Give the position of every malaria parasite.
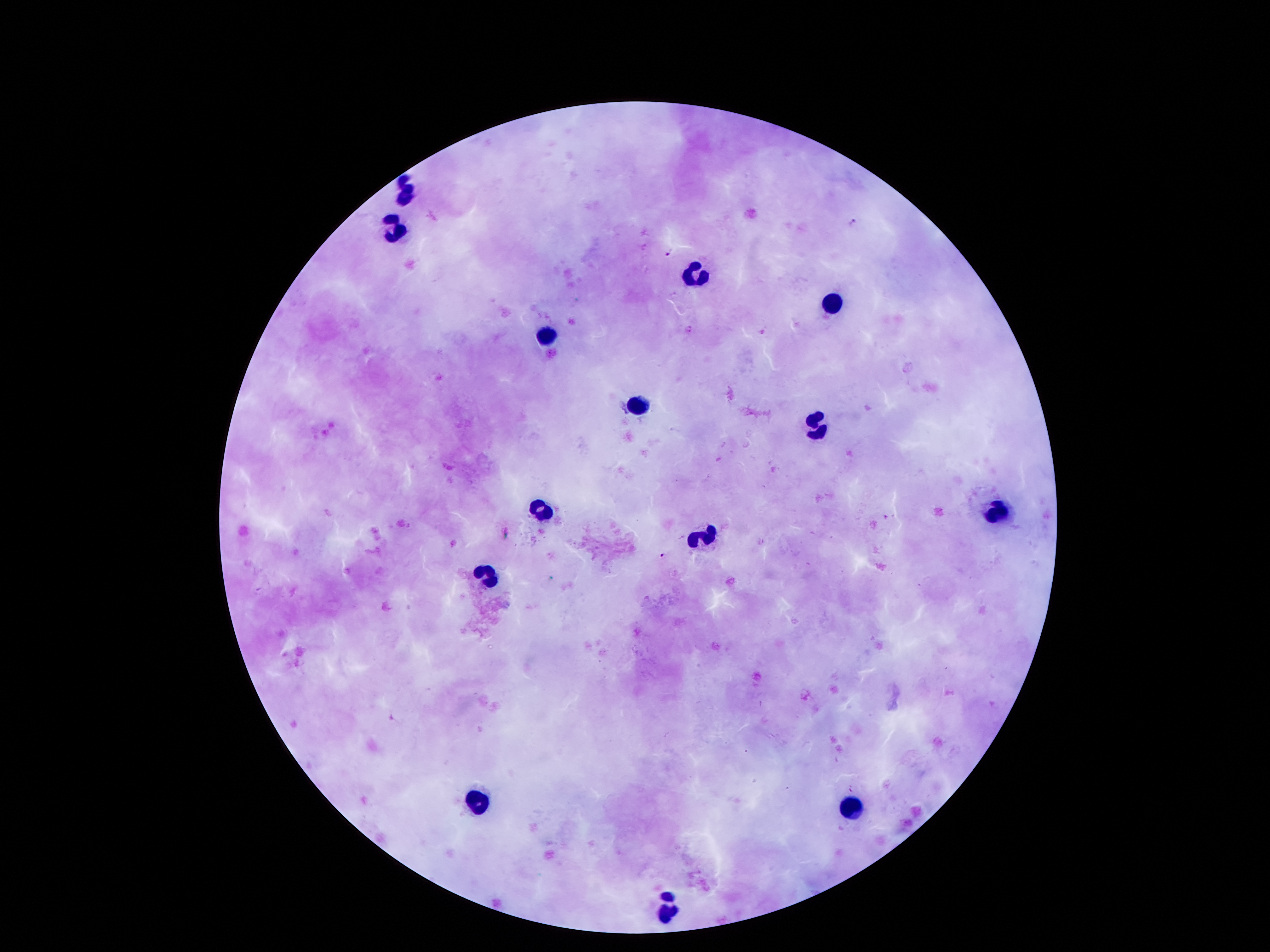
Approximate object centers, in pixels from the top-left corner.
Malaria parasites: (x=851, y=221), (x=670, y=252), (x=688, y=329), (x=662, y=554).

Leukocyte locations: (x=410, y=194), (x=396, y=226), (x=691, y=276), (x=834, y=305), (x=548, y=339), (x=637, y=407), (x=816, y=426), (x=543, y=510), (x=993, y=514), (x=700, y=539), (x=491, y=577), (x=477, y=803), (x=846, y=810), (x=668, y=912). Giemsa stain. Smartphone photograph taken through the microscope eyepiece. Image is 1270×952 pixels. Patient malaria status: infected with Plasmodium falciparum. 100x magnification. One field from this slide. Thick blood smear.